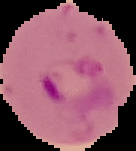

Summary:
  - Image size: 136×151 pixels
  - Image type: cell region segmented out of the field of view; surrounding area masked to black
  - Result: malaria parasites identified
  - Preparation: thin blood smear